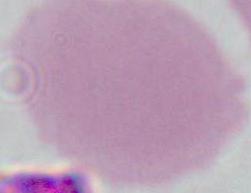

identification = red blood cell
magnification = 1000x
modality = micrograph